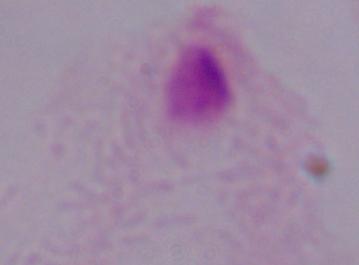
Summary:
  - Magnification: 1000x
  - Modality: micrograph
  - Identification: trichomonad